Classify this cell by malaria status.
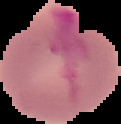
It is uninfected.

Summary:
  - Preparation: thin blood film
  - Image type: cell region segmented out of the field of view; surrounding area masked to black
  - Image size: 121×124 pixels